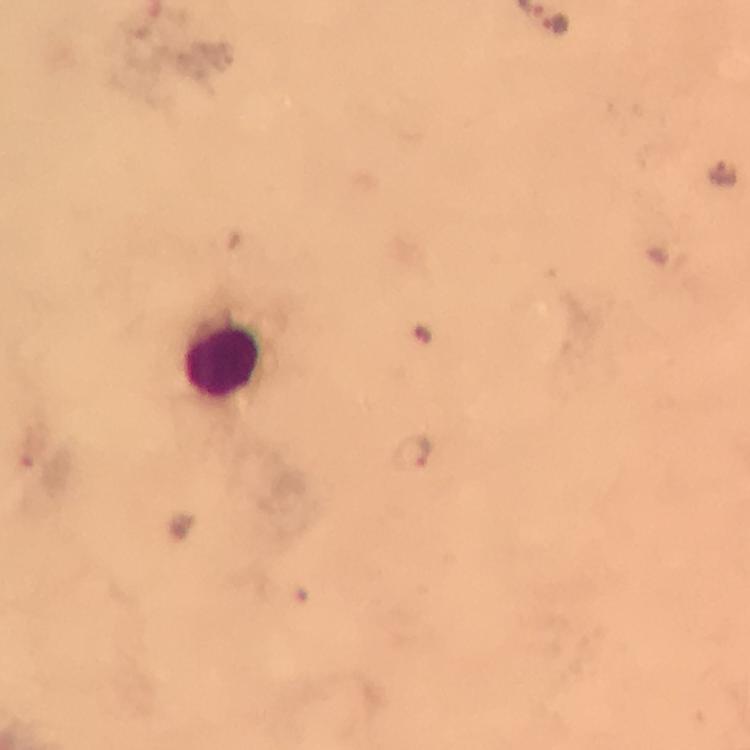
Approximate centers as {x, y} in pixels. Malaria parasite locations: {555, 25}, {721, 172}, {413, 451}. Leukocyte locations: {225, 359}. Image is 750×750 pixels. Giemsa-stained preparation. A crop from one field of view. Photographed with a smartphone mounted on the microscope. Thick blood film. At 100x magnification. From a malaria diagnostic workup. Immersion oil applied.